Classify this cell by malaria status.
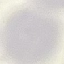

Uninfected.

Giemsa-stained preparation. Thin blood film. Cell patch, automatically extracted from a larger field of view and resized to 64 × 64 pixels. Acquired by smartphone through the microscope eyepiece.